Classify this cell by malaria status.
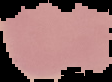
Uninfected.

image size = 112×82 pixels
preparation = thin blood film
image type = segmented cell region with the area outside set to black